Report the malaria status of this cell.
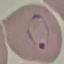

Parasitized.

Summary:
  - Capture: smartphone through the microscope eyepiece
  - Preparation: thin smear
  - Image type: cell patch, automatically extracted from a larger field of view and resized to 64 × 64 pixels
  - Stain: Giemsa